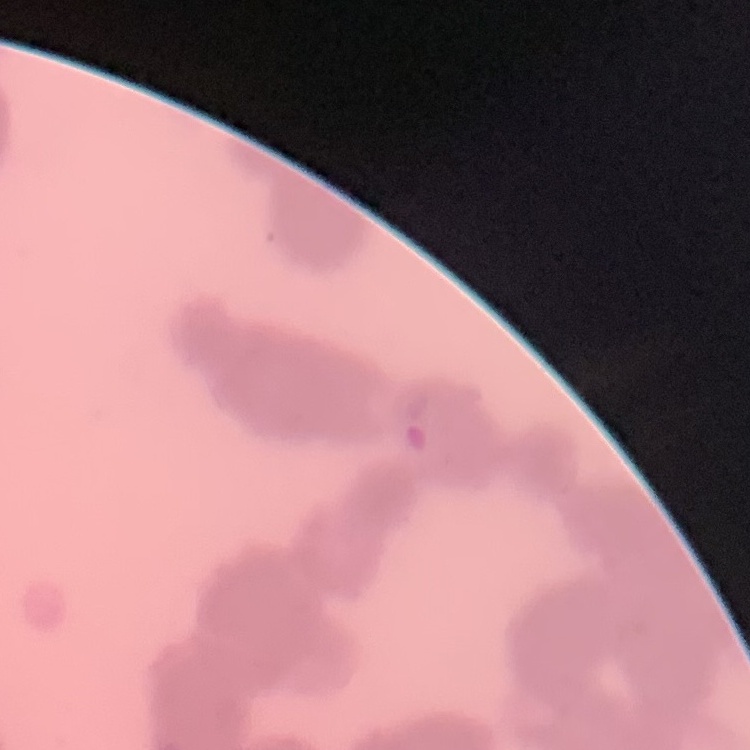 The erythrocytes exhibit rouleaux formation. Thin peripheral smear. Field's or Giemsa stain. One tile cut from a larger photomicrograph.